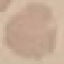
malaria status = uninfected
preparation = thin blood smear
capture = smartphone camera at the microscope eyepiece
image type = automatically extracted cell patch, resized to 64 × 64 pixels
stain = Giemsa